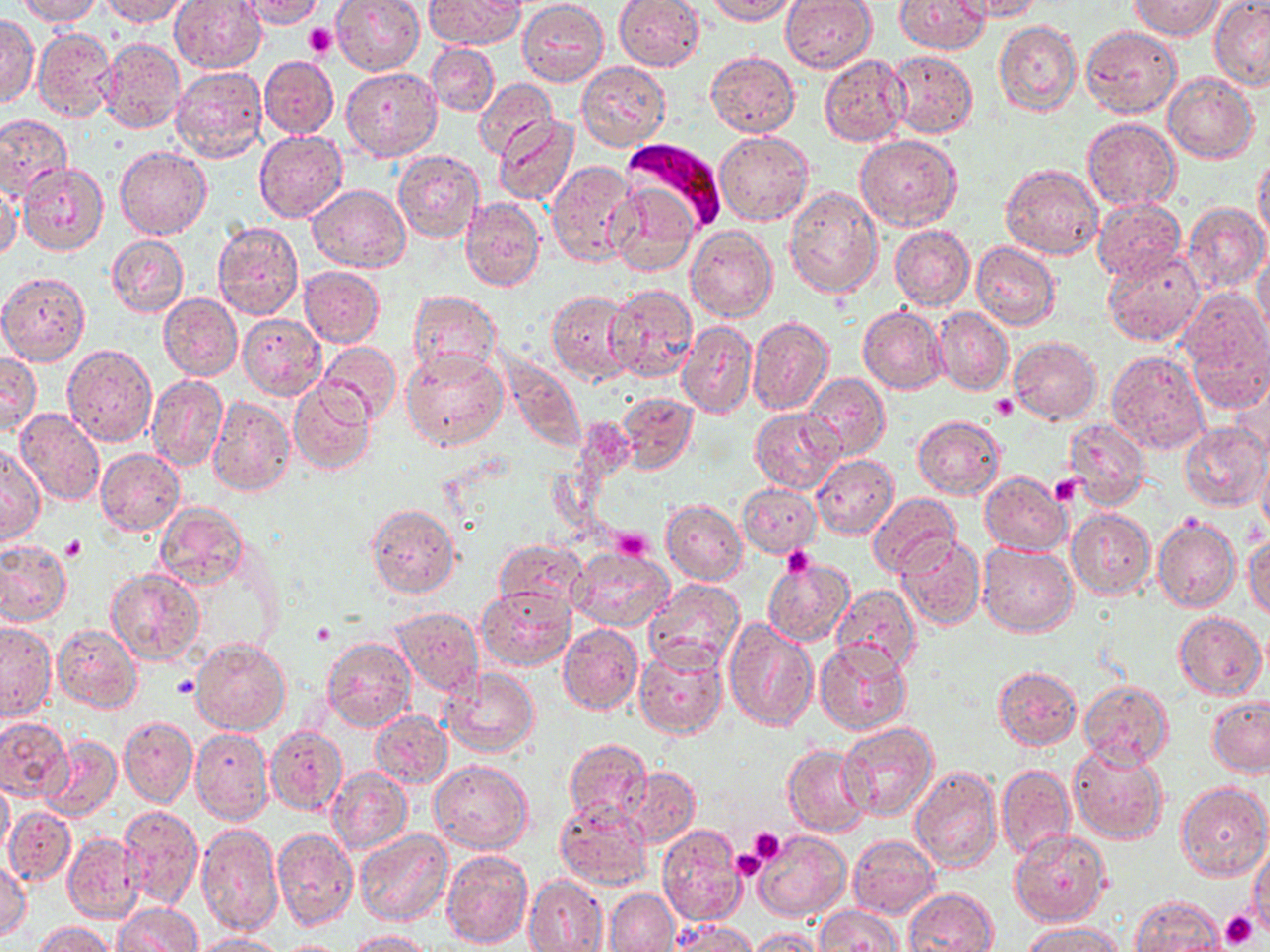
Summary:
  - Coordinate format: approximate bounding boxes as (x1, y1, x2, y2) in pixels
  - Plasmodium falciparum-infected red blood cell locations: (622, 138, 726, 232)
  - Platelet locations: (305, 24, 336, 60), (992, 394, 1018, 420), (1048, 475, 1082, 505), (612, 528, 653, 561), (62, 535, 86, 559), (782, 546, 817, 579), (172, 675, 199, 698), (747, 827, 788, 868), (731, 848, 768, 883), (1219, 913, 1258, 949)
  - Uninfected red blood cell locations: (15, 0, 101, 25), (98, 0, 192, 26), (168, 0, 266, 73), (236, 0, 328, 28), (331, 0, 424, 75), (423, 0, 526, 48), (705, 0, 802, 24), (780, 0, 877, 73), (894, 0, 992, 54), (957, 0, 1047, 22), (518, 1, 608, 85), (614, 1, 706, 71), (1131, 1, 1226, 39), (1210, 1, 1270, 89), (0, 13, 38, 108), (994, 21, 1082, 117), (1080, 25, 1183, 119), (32, 27, 117, 122), (99, 37, 185, 133), (426, 43, 499, 117), (887, 50, 978, 137), (706, 51, 799, 137), (260, 55, 338, 138), (819, 55, 910, 146), (578, 61, 670, 151), (170, 66, 267, 164), (340, 68, 442, 162), (1164, 72, 1258, 163), (474, 77, 558, 161), (0, 115, 71, 200), (494, 116, 579, 205), (1083, 118, 1180, 210), (254, 130, 348, 222), (715, 131, 813, 226), (856, 135, 962, 231), (116, 146, 211, 241), (394, 149, 485, 242), (1253, 156, 1270, 242), (547, 160, 640, 267), (17, 162, 108, 256), (1002, 164, 1103, 260), (0, 182, 22, 263), (307, 184, 410, 272), (611, 184, 698, 277), (784, 187, 883, 298), (460, 196, 546, 292), (1092, 198, 1185, 284), (1183, 202, 1268, 296), (212, 222, 304, 320), (890, 223, 974, 311), (686, 224, 777, 321), (107, 233, 189, 318), (972, 241, 1060, 330), (1103, 249, 1204, 346), (1253, 256, 1270, 344), (299, 266, 385, 347), (0, 272, 91, 366), (607, 285, 698, 381), (1176, 288, 1270, 394), (408, 289, 501, 379), (547, 291, 635, 383), (159, 294, 243, 381), (858, 307, 946, 393), (934, 308, 1013, 397), (237, 312, 326, 401), (747, 316, 833, 417), (677, 319, 757, 420), (1009, 336, 1101, 424), (316, 342, 402, 427), (62, 343, 157, 446), (401, 348, 508, 452), (1105, 350, 1209, 455), (502, 351, 586, 451), (0, 352, 40, 436), (146, 373, 227, 472), (1229, 373, 1270, 463), (805, 374, 889, 460), (168, 381, 273, 484), (289, 382, 375, 474), (616, 392, 697, 474), (208, 397, 295, 498), (15, 407, 103, 506), (749, 408, 844, 493), (912, 414, 1006, 499), (1063, 417, 1150, 507), (1180, 421, 1270, 512), (1, 445, 45, 545), (96, 448, 185, 535), (812, 454, 899, 539), (1258, 455, 1270, 541), (980, 470, 1070, 555), (738, 484, 822, 558), (868, 493, 961, 579), (661, 499, 747, 586), (154, 502, 247, 590), (365, 504, 460, 599), (1067, 509, 1155, 597), (1153, 515, 1240, 613), (1245, 533, 1269, 621), (896, 535, 985, 630), (0, 539, 72, 627), (492, 539, 588, 618), (978, 544, 1077, 636), (569, 545, 673, 631), (764, 558, 855, 647), (104, 567, 205, 665), (644, 579, 744, 674), (832, 584, 920, 673), (477, 587, 576, 672), (390, 607, 483, 695), (1173, 611, 1267, 698), (723, 619, 817, 731), (0, 622, 57, 722), (559, 623, 643, 716), (53, 624, 142, 713), (322, 637, 415, 732), (191, 638, 291, 735), (816, 641, 911, 735), (634, 643, 728, 739), (991, 666, 1083, 751), (443, 669, 539, 759), (1079, 679, 1173, 768), (1207, 695, 1270, 777), (369, 709, 451, 789), (0, 716, 72, 802), (121, 716, 196, 806), (838, 722, 938, 824), (264, 725, 347, 816), (191, 727, 274, 825), (41, 737, 121, 821), (561, 738, 651, 825), (1069, 742, 1170, 847), (783, 744, 873, 837), (430, 758, 533, 852), (910, 764, 1003, 873), (996, 765, 1075, 860), (620, 767, 700, 849), (327, 768, 411, 855), (0, 777, 13, 854), (1176, 781, 1270, 881), (555, 801, 653, 891), (118, 804, 204, 909), (4, 807, 74, 886), (197, 822, 284, 939), (270, 825, 357, 930), (657, 825, 746, 927), (1008, 828, 1110, 926), (355, 829, 453, 928), (755, 831, 851, 922), (64, 833, 144, 922), (848, 835, 939, 919), (1250, 842, 1270, 935), (121, 848, 201, 946), (441, 849, 533, 948), (0, 861, 31, 941), (524, 874, 609, 952), (904, 888, 998, 951), (606, 889, 678, 952), (1131, 895, 1226, 952), (112, 902, 202, 952), (815, 904, 902, 951), (668, 919, 755, 951), (33, 920, 116, 952), (1022, 921, 1124, 951), (748, 927, 824, 951), (345, 929, 434, 951), (190, 931, 286, 951), (279, 940, 349, 951)
  - Slide-level diagnosis: Plasmodium falciparum
  - Field of view: one of a larger specimen
  - Preparation: thin blood film
  - Image size: 1270×952 pixels
  - Modality: light microscopy
  - Magnification: 1000x
  - Stain: May-Grünwald-Giemsa